Mark where platelets are.
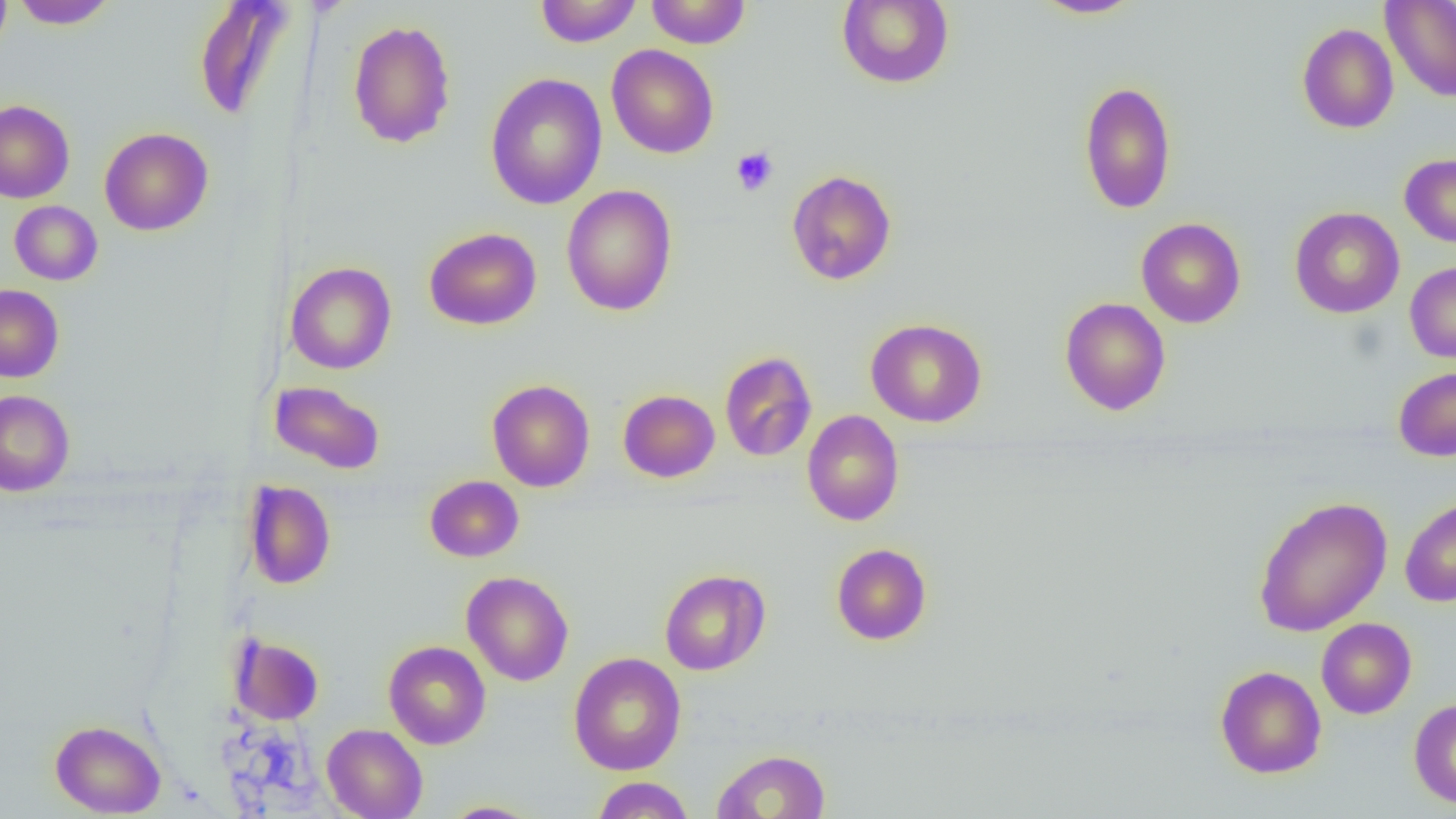
Approximate bounding boxes as [x1, y1, x2, y2] in pixels.
Platelets: [731, 147, 779, 196].

Uninfected red blood cell locations: [0, 0, 12, 57], [10, 0, 118, 29], [535, 0, 642, 47], [647, 0, 750, 48], [837, 0, 955, 89], [1028, 0, 1144, 19], [193, 1, 298, 120], [1381, 1, 1456, 102], [347, 19, 457, 149], [1297, 23, 1399, 134], [606, 44, 719, 158], [485, 72, 607, 210], [1079, 80, 1176, 214], [0, 100, 74, 203], [99, 127, 213, 235], [1399, 153, 1456, 247], [786, 169, 897, 285], [561, 185, 677, 316], [9, 201, 102, 285], [1290, 207, 1404, 318], [1136, 217, 1246, 328], [424, 227, 541, 330], [1405, 261, 1456, 363], [285, 262, 396, 374], [0, 284, 64, 383], [1059, 297, 1171, 415], [866, 318, 986, 427], [719, 351, 817, 461], [1393, 366, 1456, 461], [487, 379, 595, 492], [270, 380, 386, 474], [618, 389, 720, 482], [0, 390, 75, 496], [802, 410, 904, 526], [424, 475, 524, 562], [244, 480, 336, 589], [1253, 495, 1393, 637], [1400, 495, 1456, 607], [831, 543, 932, 645], [659, 569, 771, 675], [461, 571, 574, 686], [1316, 618, 1416, 719], [229, 633, 324, 725], [383, 640, 491, 749], [568, 652, 686, 775], [1215, 665, 1326, 778], [1408, 697, 1456, 809], [50, 719, 165, 817], [321, 723, 428, 819], [711, 750, 831, 818], [592, 776, 695, 818], [438, 801, 544, 818]. Slide-level diagnosis: no evidence of blood parasites. One field of a larger specimen. Thin blood film. Captured at 1000x magnification. Image is 1456×819 pixels. Light microscopy.